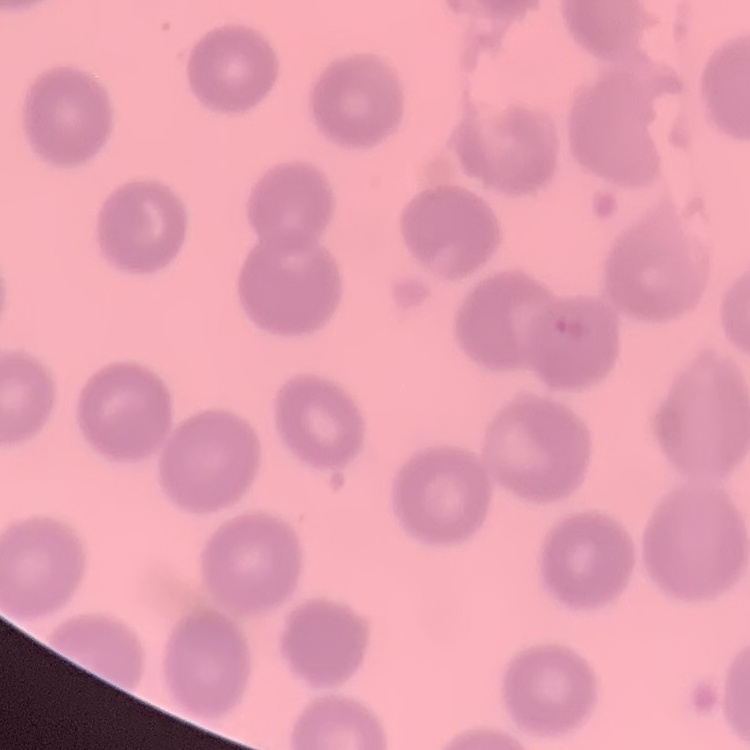
The red blood cells show no rouleaux formation. Square crop of a larger photomicrograph. Thin blood film. Field's or Giemsa stain.